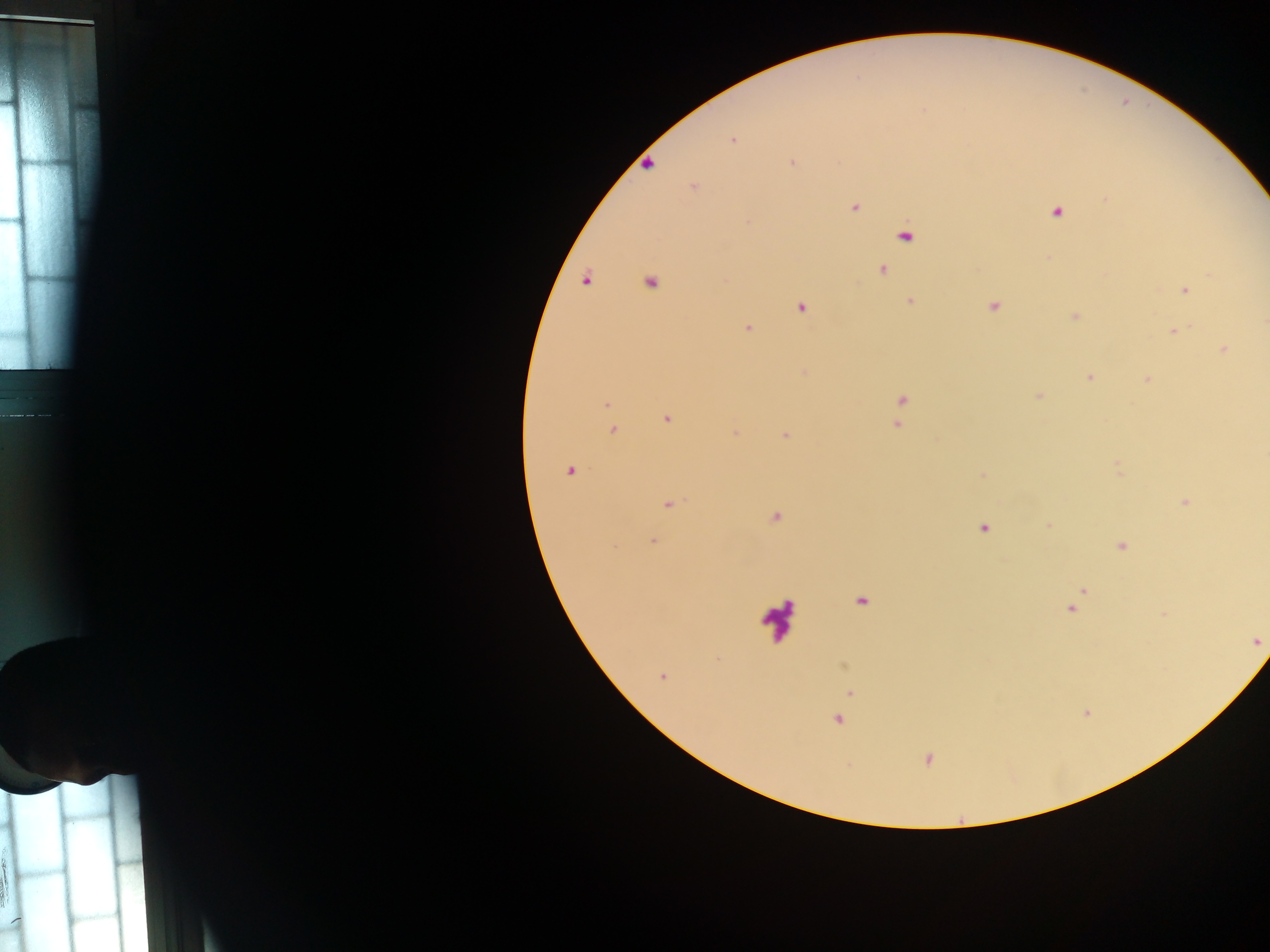
Approximate centers as (x, y) in pixels.
Summary:
  - Malaria parasite locations: (732, 141), (792, 163), (649, 165), (694, 187), (1107, 199), (855, 208), (1057, 213), (749, 222), (905, 235), (883, 271), (585, 281), (650, 283), (1184, 290), (910, 301), (993, 306), (801, 308), (1075, 316), (1264, 323), (748, 328), (1173, 331), (1225, 350), (1090, 378), (1146, 379), (902, 400), (606, 404), (666, 418), (897, 425), (613, 429), (734, 433), (785, 434), (569, 471), (982, 475), (1185, 502), (669, 504), (775, 517), (1049, 525), (984, 528), (653, 541), (1121, 546), (1082, 591), (861, 601), (1071, 608), (661, 677), (850, 693), (838, 720), (929, 759)
  - Leukocyte locations: (777, 618)
  - Country: Ghana
  - Preparation: thick blood smear
  - Capture: mobile-phone photograph through a microscope
  - Field of view: single
  - Image size: 1270×952 pixels